Locate every malaria parasite.
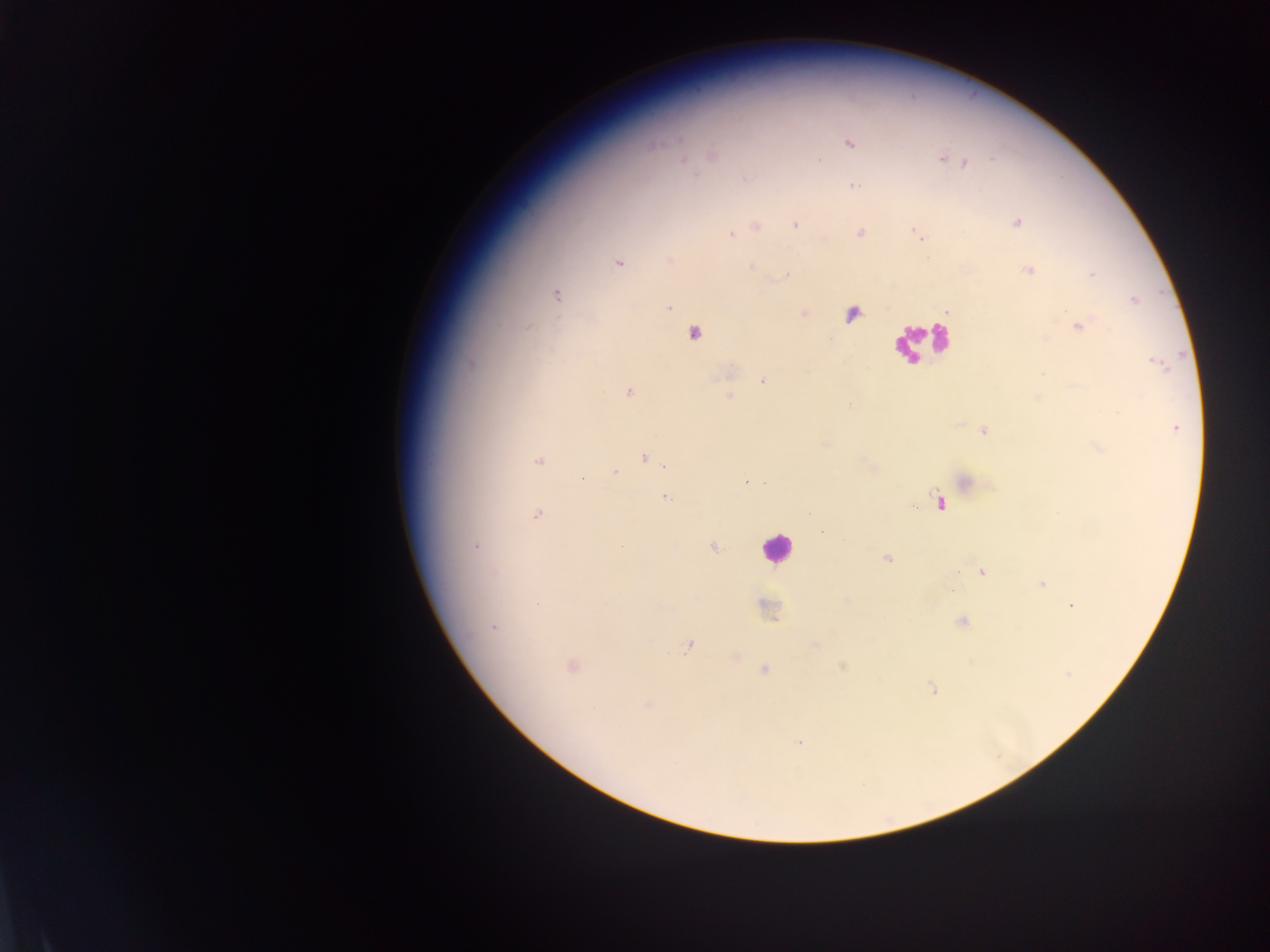

Approximate centers as (x, y) in pixels.
Malaria parasites: (849, 143), (712, 154), (941, 158), (819, 160), (684, 161), (966, 163), (746, 177), (852, 185), (1017, 222), (796, 224), (755, 225), (860, 232), (916, 233), (731, 234), (670, 259), (618, 262), (751, 265), (1028, 270), (787, 274), (555, 294), (1133, 299), (668, 308), (948, 310), (803, 313), (852, 314), (1078, 325), (694, 332), (729, 372), (764, 380), (629, 392), (728, 395), (849, 405), (1175, 427), (983, 430), (825, 443), (643, 456), (539, 461), (665, 465), (872, 468), (613, 472), (746, 483), (965, 483), (664, 497), (941, 502), (911, 505), (537, 514), (823, 532), (620, 545), (474, 546), (712, 547), (886, 558), (982, 572), (1042, 583), (845, 602), (1071, 605), (766, 608), (962, 621), (494, 627), (814, 645), (689, 646), (734, 657), (570, 665), (844, 666), (764, 669), (932, 690), (647, 705), (799, 741).

field_of_view: single
country: Ghana
preparation: thick blood smear
leukocyte_locations: 'approximate centers as (x, y) in pixels: (919, 341), (776, 548)'
capture: mobile-phone photograph through a microscope
image_size: 1270×952 pixels